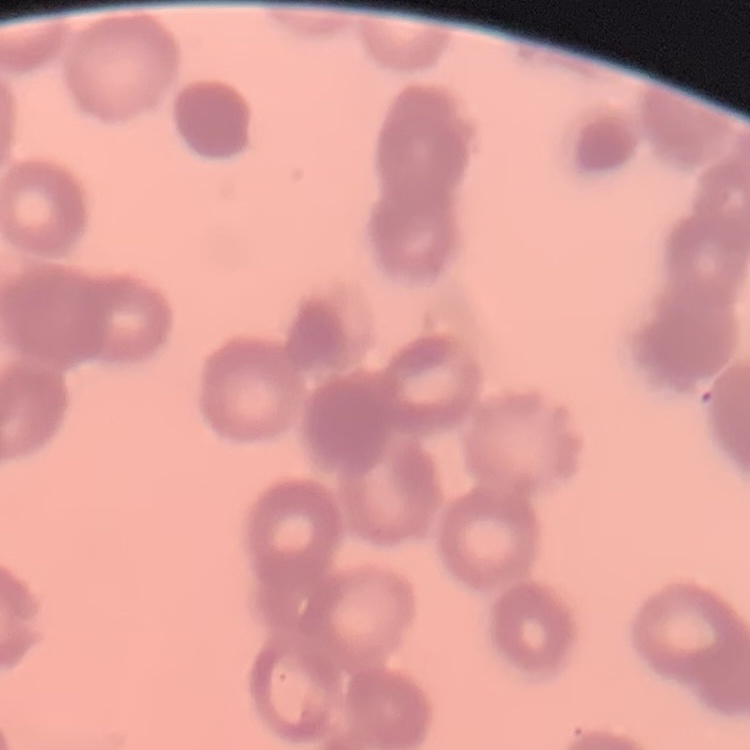

The red blood cells show rouleaux formation. One tile cut from a larger photomicrograph. Thin blood smear. Field's or Giemsa stain.